Give a bounding box for every Plasmodium parasite.
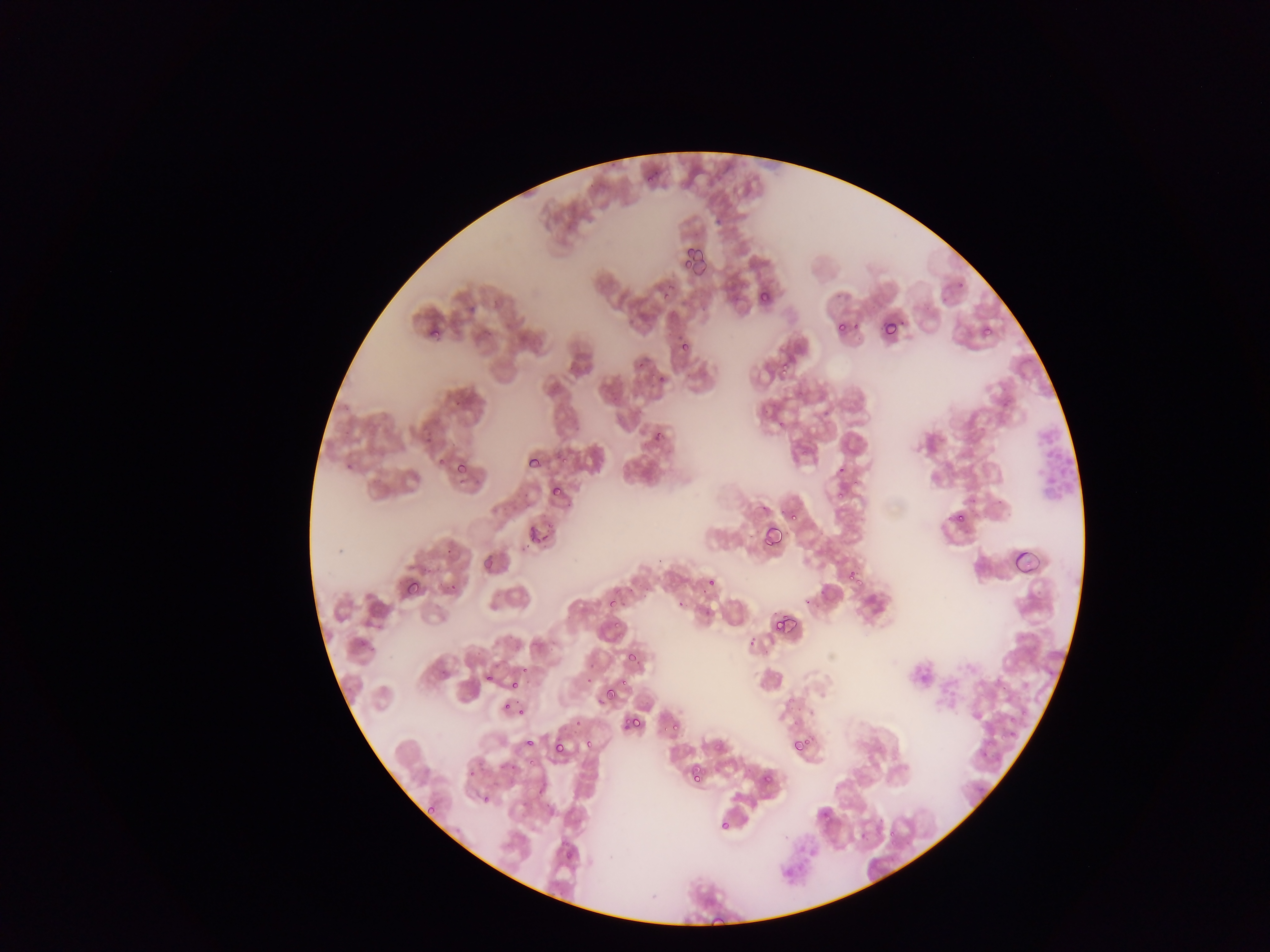
Approximate bounding boxes as [left, top, right, bottom] in pixels.
Plasmodium parasites: [646, 177, 655, 183], [683, 247, 696, 259], [693, 252, 711, 283], [683, 261, 692, 269], [667, 285, 680, 293], [760, 290, 771, 303], [663, 294, 674, 302], [882, 319, 895, 338], [837, 322, 847, 331], [981, 323, 994, 337], [430, 329, 442, 336], [681, 344, 693, 352], [781, 360, 794, 373], [660, 375, 665, 386], [658, 428, 665, 438], [562, 457, 570, 463], [528, 458, 545, 469], [452, 464, 467, 473], [851, 479, 859, 488], [550, 485, 562, 495], [835, 494, 845, 500], [953, 513, 968, 527], [788, 514, 800, 522], [525, 524, 535, 535], [762, 526, 784, 549], [543, 531, 550, 547], [530, 535, 541, 546], [482, 557, 493, 569], [846, 570, 857, 582], [706, 579, 716, 585], [855, 579, 865, 590], [407, 580, 421, 596], [607, 597, 620, 609], [773, 603, 801, 630], [611, 622, 623, 629], [617, 630, 628, 638], [627, 654, 638, 665], [522, 666, 530, 672], [486, 675, 496, 681], [620, 677, 631, 691], [511, 679, 520, 688], [605, 689, 616, 703], [597, 697, 606, 705], [503, 702, 511, 710], [519, 706, 526, 717], [623, 715, 632, 730], [631, 717, 642, 727], [671, 719, 682, 734], [1010, 719, 1018, 725], [662, 725, 670, 731], [1011, 731, 1020, 736], [1000, 733, 1012, 744], [586, 736, 599, 747], [525, 737, 535, 748], [789, 738, 808, 756], [552, 740, 565, 756], [713, 741, 723, 753], [528, 760, 538, 768], [509, 761, 519, 771], [690, 765, 701, 784], [469, 769, 476, 778], [764, 773, 772, 786], [484, 796, 489, 807], [426, 804, 439, 814], [720, 820, 731, 830], [886, 828, 894, 836], [565, 852, 573, 860], [710, 911, 726, 927].

Leukocyte locations: [1033, 424, 1075, 504]. Image is 1270×952 pixels. Mobile-phone photograph taken through the microscope. Sample from Ghana. Thin blood film. Single field of view.